Outline each blood parasite and name the species.
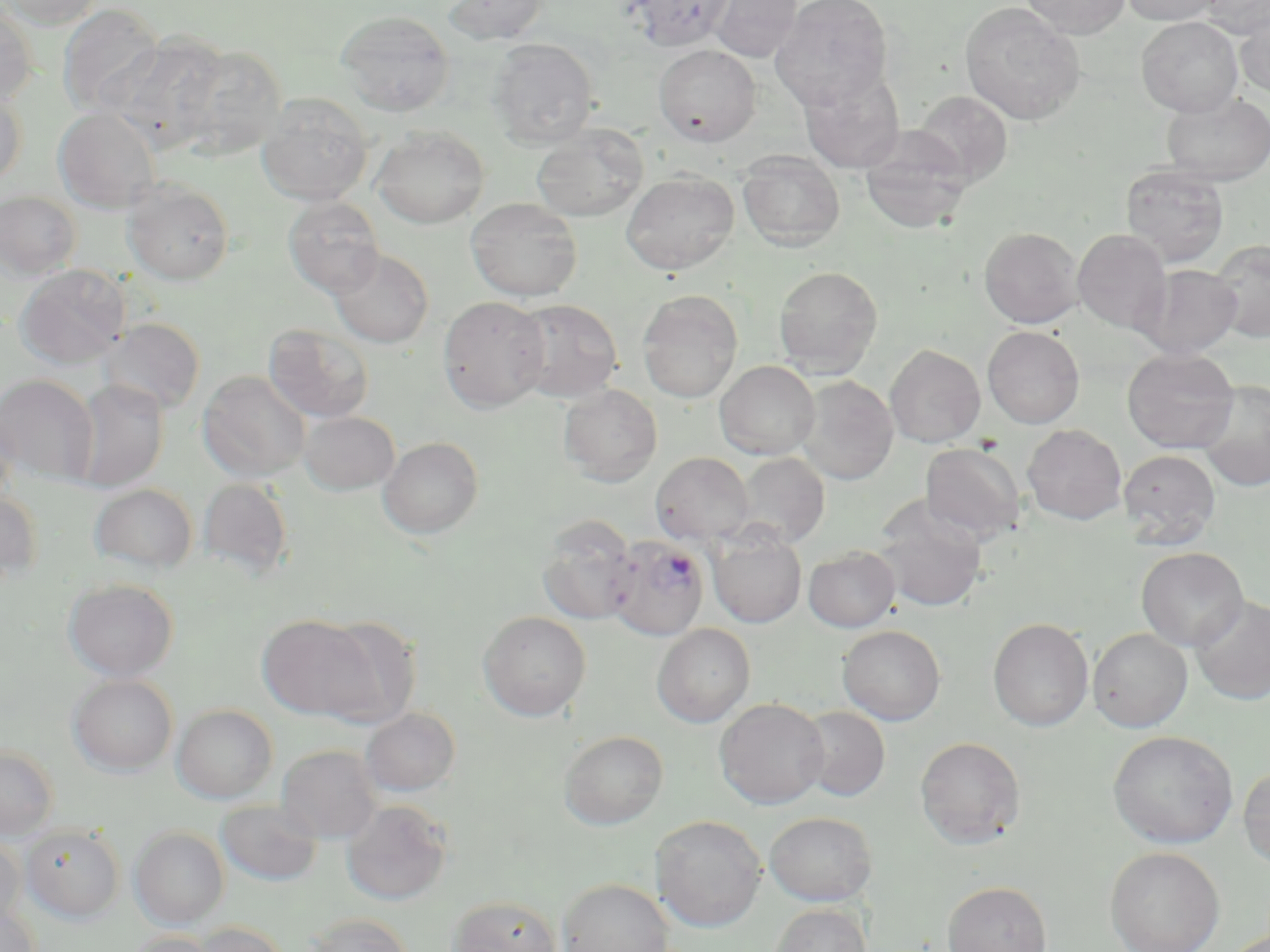

Approximate bounding boxes as [x1, y1, x2, y2] in pixels.
Plasmodium falciparum-infected red blood cells: [606, 535, 709, 641].
No Plasmodium ovale, Plasmodium malariae, Plasmodium vivax, Babesia divergens, or Trypanosoma brucei observed.

Summary:
  - Uninfected red blood cell locations: [2, 0, 104, 29], [443, 0, 549, 45], [708, 0, 803, 63], [771, 0, 894, 111], [1020, 0, 1130, 38], [1120, 0, 1224, 25], [1199, 0, 1270, 36], [959, 2, 1086, 125], [0, 3, 39, 106], [57, 3, 164, 117], [1235, 5, 1270, 98], [335, 11, 455, 116], [1137, 16, 1243, 117], [108, 32, 228, 150], [488, 38, 599, 148], [177, 43, 288, 159], [654, 44, 761, 146], [799, 69, 905, 173], [0, 89, 27, 186], [911, 90, 1013, 187], [256, 92, 374, 205], [1162, 92, 1270, 185], [53, 107, 162, 213], [531, 124, 649, 222], [372, 125, 490, 229], [858, 129, 972, 235], [737, 151, 845, 252], [1120, 164, 1230, 267], [621, 171, 739, 275], [122, 178, 235, 285], [0, 191, 81, 280], [282, 196, 385, 297], [466, 197, 583, 302], [979, 226, 1084, 328], [1073, 229, 1172, 335], [1209, 239, 1270, 342], [328, 247, 434, 348], [15, 264, 130, 369], [1138, 264, 1242, 358], [773, 265, 884, 377], [637, 290, 743, 403], [437, 295, 551, 412], [509, 299, 624, 403], [99, 318, 205, 416], [263, 323, 375, 423], [983, 326, 1084, 429], [885, 344, 985, 448], [1122, 348, 1240, 453], [714, 360, 820, 460], [198, 370, 311, 482], [0, 374, 98, 485], [795, 375, 899, 485], [70, 379, 169, 491], [1198, 379, 1270, 493], [558, 384, 663, 487], [0, 403, 20, 506], [298, 411, 400, 495], [1022, 424, 1127, 525], [378, 437, 484, 538], [920, 443, 1026, 545], [1118, 449, 1221, 549], [650, 452, 755, 546], [733, 452, 830, 549], [197, 478, 295, 578], [89, 483, 198, 573], [0, 491, 43, 583], [873, 501, 988, 612], [536, 515, 639, 626], [708, 528, 806, 627], [803, 546, 900, 632], [1136, 547, 1248, 651], [64, 578, 178, 681], [1190, 595, 1270, 705], [478, 610, 592, 721], [258, 615, 378, 720], [313, 616, 422, 727], [988, 617, 1094, 731], [651, 624, 755, 727], [837, 625, 946, 725], [1088, 627, 1193, 732], [68, 674, 177, 775], [714, 698, 829, 809], [172, 704, 277, 803], [798, 706, 890, 801], [360, 707, 461, 797], [559, 730, 668, 830], [1108, 730, 1238, 848], [915, 736, 1027, 849], [0, 744, 59, 840], [276, 744, 383, 843], [1238, 763, 1270, 871], [216, 799, 322, 886], [341, 799, 453, 906], [764, 811, 878, 906], [650, 815, 767, 932], [20, 824, 125, 922], [130, 827, 229, 928], [0, 834, 26, 929], [1104, 846, 1225, 952], [557, 878, 674, 952], [942, 880, 1052, 952], [448, 895, 563, 952], [0, 900, 41, 952], [768, 902, 873, 952], [305, 913, 415, 952], [187, 922, 289, 952], [123, 930, 219, 952]
  - Slide-level diagnosis: Plasmodium falciparum
  - Image size: 1270×952 pixels
  - Stain: May-Grünwald-Giemsa
  - Modality: optical microscopy
  - Field of view: one of a larger specimen
  - Preparation: thin blood film
  - Magnification: 1000x